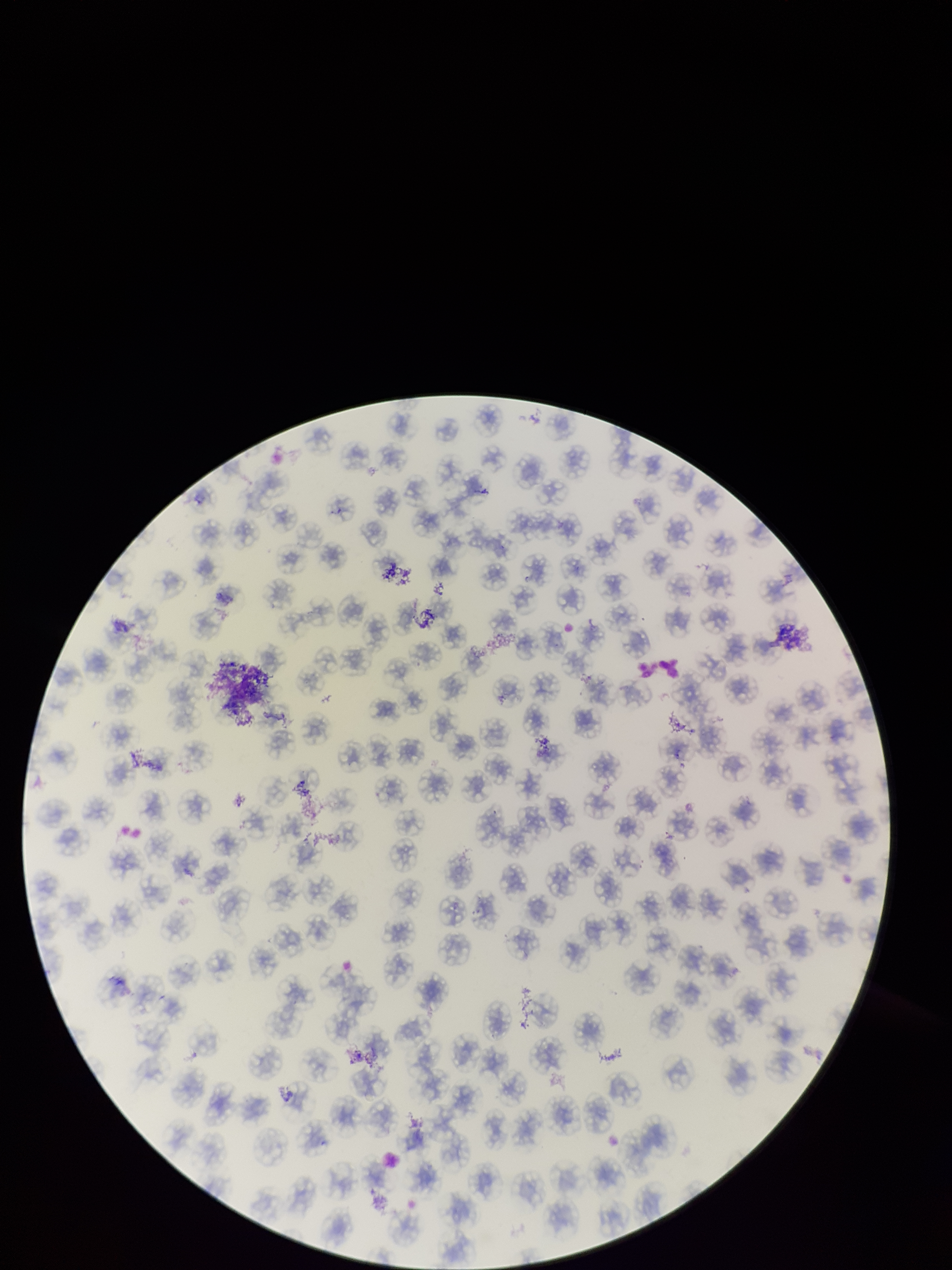

preparation = thin blood smear
stain = Giemsa
image size = 952×1270 pixels
parasitized red blood cell count = 0
field of view = one from this slide
capture = smartphone photograph through the microscope eyepiece
patient malaria status = negative
red blood cell count = 145
parasitized red blood cells = none identified